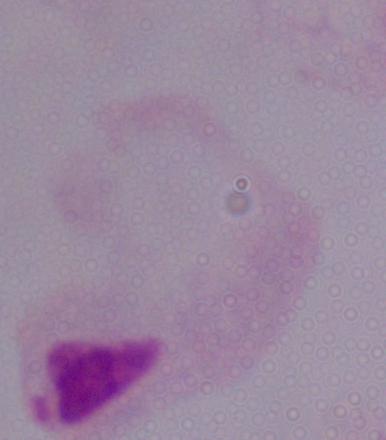
{
  "identification": "trichomonad",
  "modality": "photomicrograph",
  "magnification": "1000x"
}